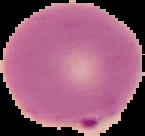
Summary:
  - Image type: segmented cell region on a black background
  - Preparation: thin blood film
  - Image size: 145×136 pixels
  - Result: malaria parasites detected